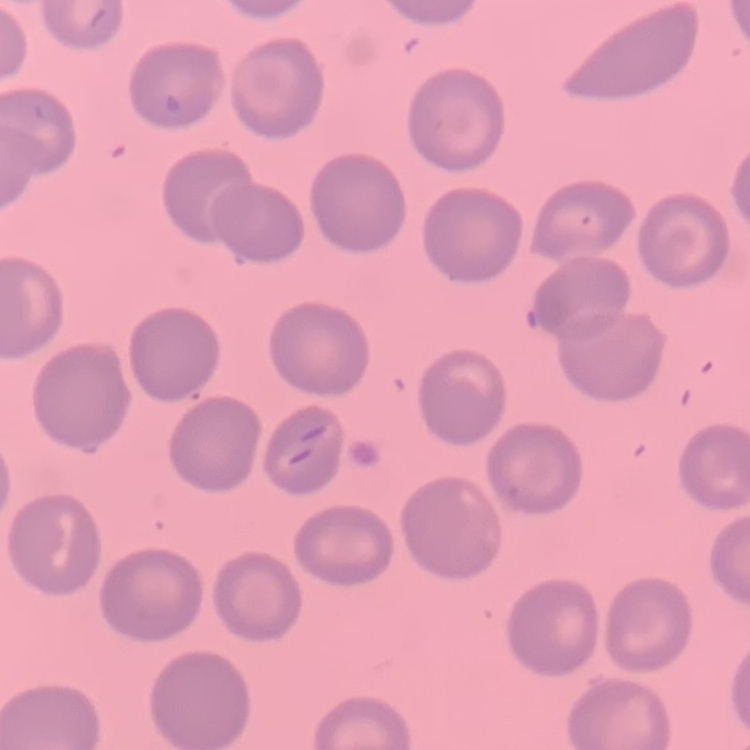

erythrocyte morphology = no rouleaux formation
preparation = thin blood smear
stain = Field's or Giemsa
image type = one tile cut from a larger photomicrograph